Locate every blood parasite and identify its species.
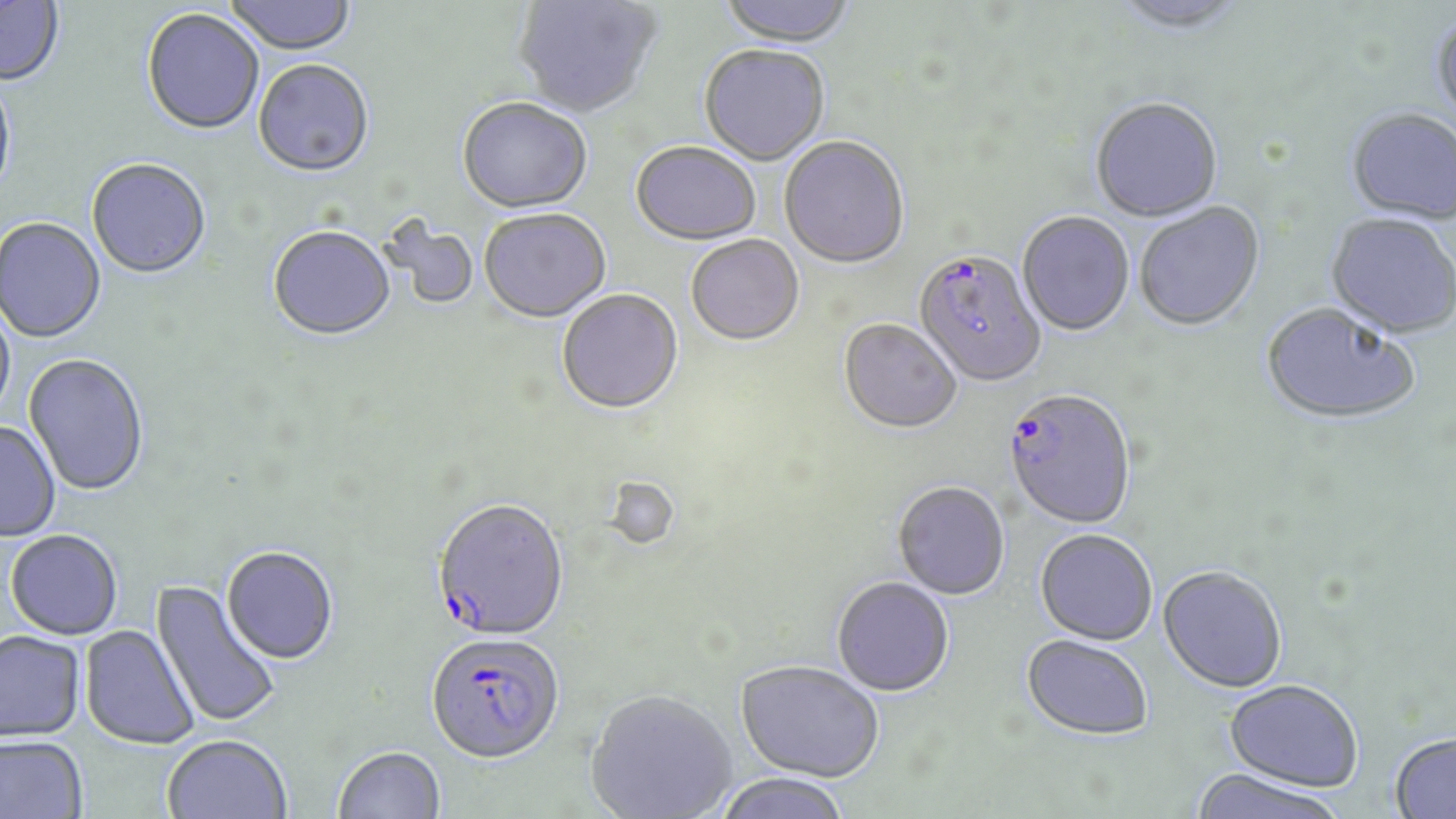
Approximate bounding boxes as (x1,y1)-(x2,y2) corner pairs in pixels.
Plasmodium falciparum-infected red blood cells: (913,252)-(1046,390), (1002,392)-(1136,531), (431,499)-(569,642), (426,631)-(565,762).
No Plasmodium ovale, Plasmodium malariae, Plasmodium vivax, Babesia divergens, or Trypanosoma brucei observed.

Uninfected red blood cell locations: (224,0)-(356,58), (513,0)-(662,120), (716,0)-(858,50), (0,1)-(64,87), (1109,1)-(1250,37), (141,10)-(264,137), (1430,14)-(1456,135), (698,47)-(830,167), (253,61)-(374,180), (0,76)-(17,207), (456,99)-(592,216), (1091,100)-(1223,224), (1345,110)-(1456,228), (779,138)-(909,271), (629,144)-(762,248), (86,160)-(211,281), (1135,203)-(1266,333), (479,210)-(611,325), (1017,213)-(1134,338), (1324,215)-(1456,341), (384,216)-(479,311), (0,218)-(106,344), (267,228)-(396,343), (686,237)-(804,347), (557,290)-(684,416), (0,299)-(16,424), (1260,305)-(1420,428), (838,320)-(961,436), (23,354)-(149,497), (0,421)-(61,542), (892,483)-(1010,602), (6,530)-(123,640), (1035,531)-(1158,648), (222,546)-(339,664), (1158,568)-(1287,695), (832,578)-(954,698), (150,579)-(283,730), (79,624)-(199,749), (0,630)-(85,741), (1021,636)-(1153,742), (735,660)-(884,782), (1223,682)-(1363,793), (585,688)-(737,819), (162,734)-(292,819), (1390,734)-(1456,819), (0,735)-(88,819), (333,745)-(446,819), (1187,769)-(1347,819), (713,773)-(852,819). Slide-level diagnosis: Plasmodium falciparum. One field of a larger specimen. Image is 1456×819 pixels. 1000x magnification. Thin blood film. Optical microscopy. May-Grünwald-Giemsa stain.